Name the parasite shown.
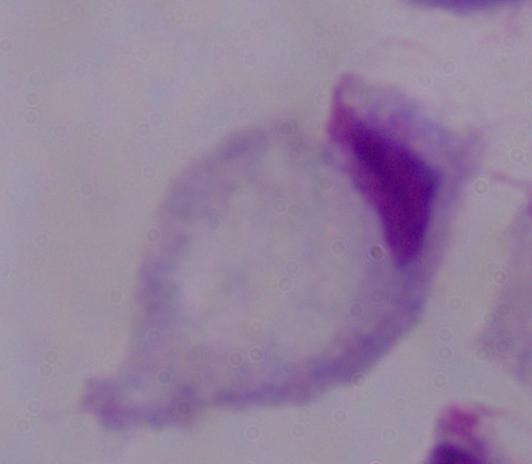
This is a trichomonad.

{
  "magnification": "1000x",
  "modality": "micrograph"
}